Evaluate for malaria.
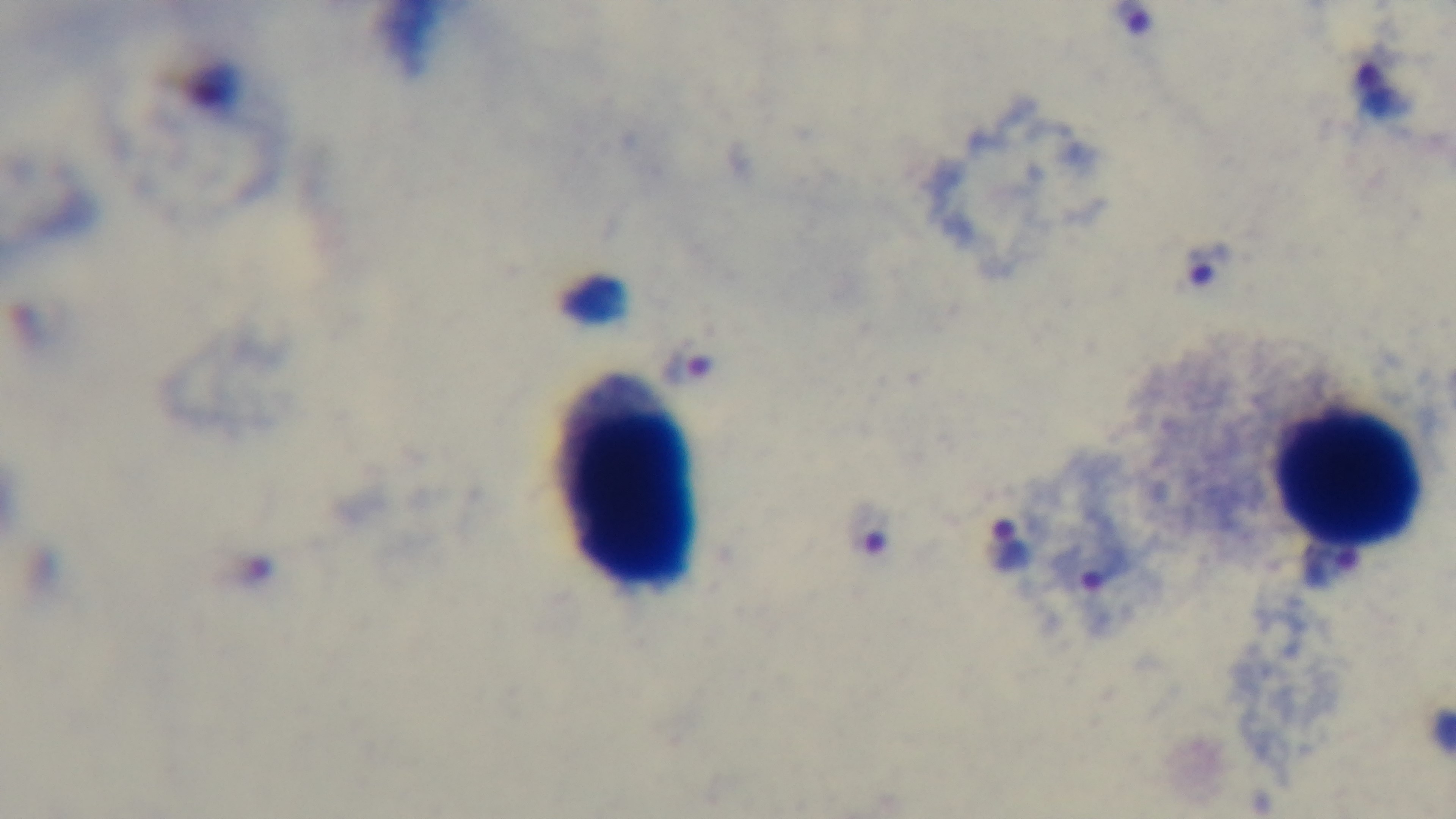
Positive.

objective: 100x oil immersion
capture: mounted 4K digital camera
modality: light microscopy
preparation: thick
field_of_view: one from the slide
stain: Giemsa